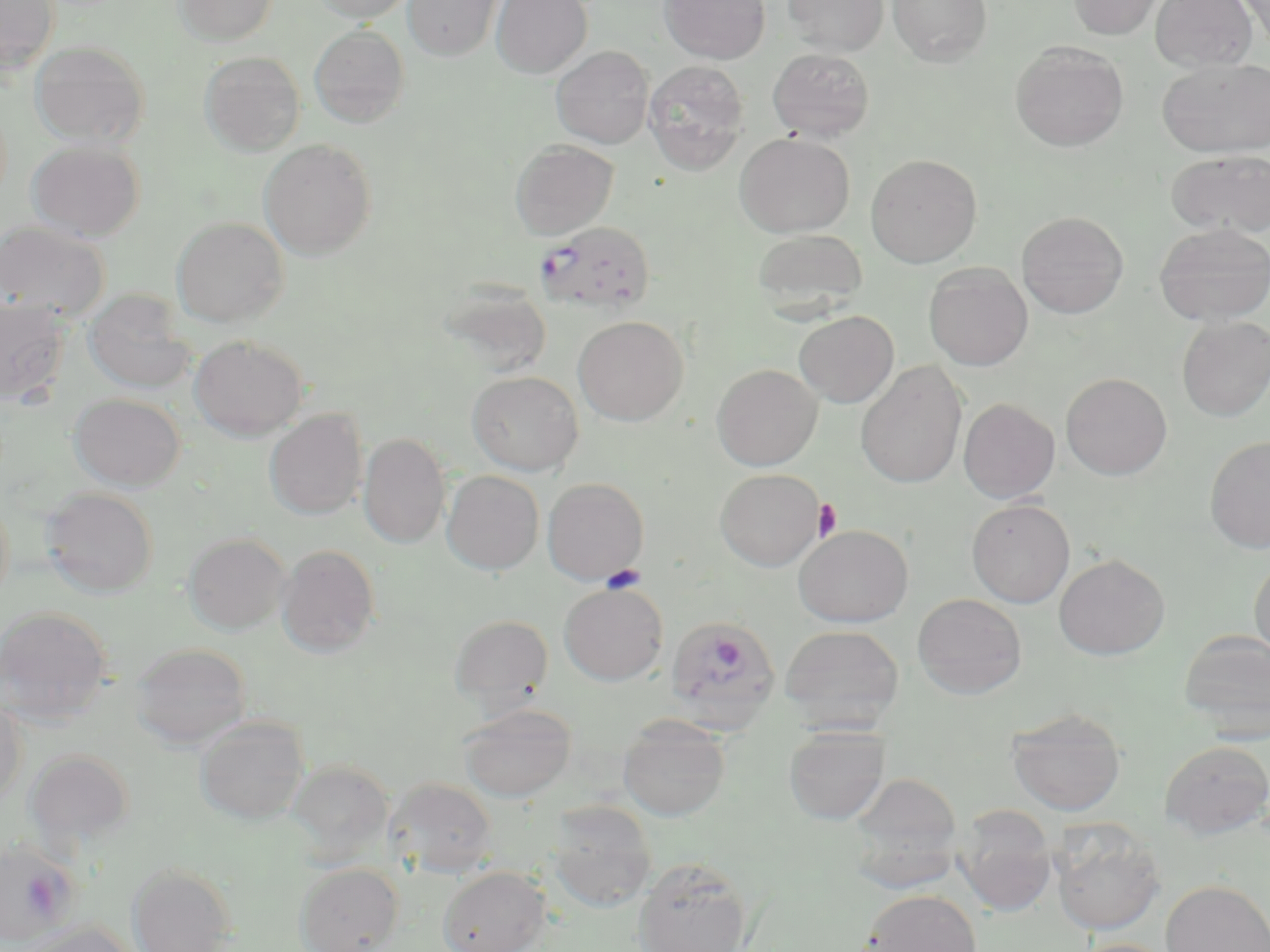

slide-level diagnosis = Plasmodium falciparum
stain = May-Grünwald-Giemsa
uninfected red blood cell locations = approximate bounding boxes as [x1, y1, x2, y2] in pixels: [0, 0, 60, 76], [173, 0, 278, 46], [310, 0, 416, 23], [403, 0, 504, 61], [491, 0, 592, 78], [659, 0, 770, 64], [782, 0, 889, 56], [887, 0, 993, 66], [1067, 0, 1165, 39], [1150, 0, 1257, 71], [1237, 0, 1270, 49], [309, 25, 409, 128], [30, 40, 150, 148], [1010, 42, 1129, 151], [551, 46, 654, 149], [767, 47, 875, 142], [199, 51, 305, 156], [1157, 58, 1270, 158], [642, 59, 750, 175], [734, 132, 855, 237], [27, 139, 145, 241], [259, 139, 377, 260], [509, 139, 619, 240], [1166, 149, 1270, 238], [865, 153, 982, 267], [1017, 211, 1128, 318], [171, 216, 290, 327], [0, 220, 110, 322], [1154, 222, 1270, 325], [752, 228, 868, 316], [923, 263, 1033, 371], [438, 285, 553, 381], [82, 288, 197, 394], [0, 297, 71, 405], [794, 310, 899, 407], [1177, 315, 1270, 421], [573, 316, 689, 425], [189, 334, 309, 440], [855, 361, 968, 488], [711, 363, 823, 470], [466, 370, 583, 476], [1061, 372, 1172, 480], [68, 392, 186, 490], [958, 397, 1060, 503], [264, 408, 368, 520], [359, 432, 450, 549], [1204, 435, 1270, 554], [715, 468, 826, 570], [441, 470, 544, 574], [542, 477, 649, 585], [41, 488, 159, 597], [0, 490, 13, 609], [966, 498, 1075, 608], [794, 525, 914, 627], [183, 532, 291, 635], [276, 544, 380, 657], [1053, 553, 1170, 660], [1249, 555, 1270, 662], [559, 582, 668, 685], [912, 593, 1027, 699], [0, 605, 113, 725], [449, 614, 553, 709], [780, 624, 904, 729], [1179, 629, 1270, 740], [131, 643, 251, 748], [0, 696, 26, 811], [459, 703, 576, 802], [1006, 708, 1126, 815], [618, 715, 731, 821], [194, 716, 310, 825], [783, 725, 890, 825], [1160, 740, 1270, 838], [25, 749, 135, 850], [287, 759, 394, 864], [847, 771, 964, 886], [386, 777, 498, 877], [547, 801, 657, 912], [954, 805, 1057, 916], [1050, 818, 1166, 936], [633, 857, 752, 952], [127, 862, 239, 952], [294, 862, 404, 952], [437, 865, 550, 952], [1161, 879, 1270, 952], [862, 888, 982, 952], [21, 922, 139, 952], [1069, 938, 1178, 952]
image size = 1270×952 pixels
preparation = thin blood film
magnification = 1000x
platelet locations = approximate bounding boxes as [x1, y1, x2, y2] in pixels: [813, 499, 842, 542], [601, 564, 647, 593]
field of view = one of a larger specimen
modality = light microscopy
Plasmodium falciparum-infected red blood cell locations = approximate bounding boxes as [x1, y1, x2, y2] in pixels: [536, 220, 656, 311], [668, 617, 782, 737], [0, 842, 81, 947]